Identify the blood parasite species.
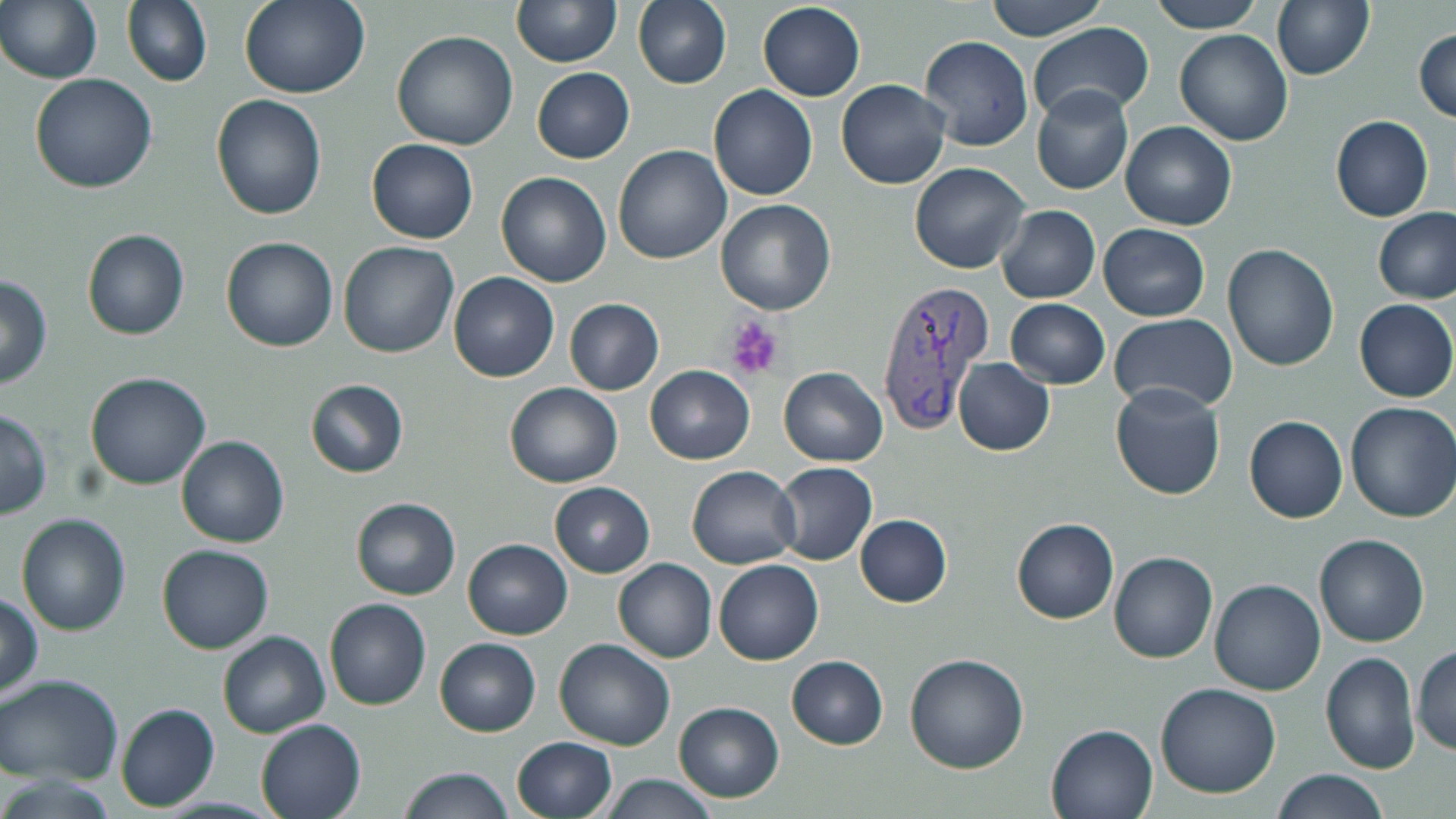
Plasmodium vivax.

magnification = 1000x
uninfected red blood cell locations = approximate bounding boxes as (x1, y1, x2, y2) in pixels: (122, 0, 212, 88), (239, 0, 369, 99), (511, 0, 619, 67), (632, 0, 732, 90), (985, 0, 1106, 39), (1149, 0, 1263, 33), (1271, 1, 1375, 80), (1, 2, 101, 84), (757, 2, 866, 100), (1026, 22, 1152, 127), (1413, 28, 1456, 121), (1174, 29, 1293, 146), (391, 30, 519, 150), (919, 35, 1033, 151), (532, 67, 635, 163), (30, 74, 158, 193), (835, 77, 951, 190), (1031, 84, 1134, 195), (708, 85, 817, 201), (208, 94, 328, 221), (1331, 115, 1432, 222), (1120, 121, 1237, 230), (365, 138, 479, 244), (611, 145, 732, 264), (909, 162, 1031, 274), (495, 172, 613, 289), (714, 199, 837, 314), (996, 204, 1100, 304), (1372, 207, 1455, 307), (1099, 224, 1210, 320), (81, 229, 190, 341), (219, 236, 339, 352), (338, 240, 460, 359), (1222, 243, 1339, 370), (449, 271, 559, 382), (0, 272, 52, 389), (563, 299, 665, 396), (1005, 299, 1111, 389), (1354, 299, 1455, 403), (1109, 314, 1236, 412), (953, 357, 1055, 456), (645, 365, 755, 464), (779, 367, 888, 467), (86, 372, 211, 491), (304, 379, 410, 478), (504, 382, 623, 488), (1110, 382, 1226, 500), (1346, 400, 1456, 523), (0, 408, 51, 520), (1244, 414, 1347, 523), (176, 435, 289, 548), (774, 462, 877, 565), (685, 466, 802, 569), (549, 482, 655, 577), (350, 497, 461, 600), (15, 513, 132, 636), (855, 514, 952, 608), (1011, 517, 1119, 624), (1313, 534, 1429, 647), (462, 539, 573, 639), (156, 543, 273, 654), (1108, 551, 1218, 664), (612, 558, 716, 663), (713, 559, 823, 665), (1209, 579, 1326, 696), (1, 593, 43, 699), (324, 598, 431, 711), (218, 630, 330, 738), (435, 638, 541, 737), (552, 639, 675, 751), (1412, 644, 1456, 759), (904, 652, 1031, 774), (1321, 652, 1420, 774), (785, 655, 889, 749), (0, 673, 124, 786), (1155, 682, 1282, 799), (673, 701, 784, 802), (115, 703, 220, 812), (255, 718, 366, 819), (1046, 722, 1160, 818), (512, 736, 617, 819), (397, 767, 513, 819), (1273, 769, 1389, 818), (599, 775, 720, 817)
stain = May-Grünwald-Giemsa
preparation = thin blood film
image size = 1456×819 pixels
Plasmodium vivax-infected red blood cell locations = approximate bounding boxes as (x1, y1, x2, y2) in pixels: (873, 279, 994, 436)
modality = light microscopy
field of view = single
platelet locations = approximate bounding boxes as (x1, y1, x2, y2) in pixels: (725, 314, 787, 380)